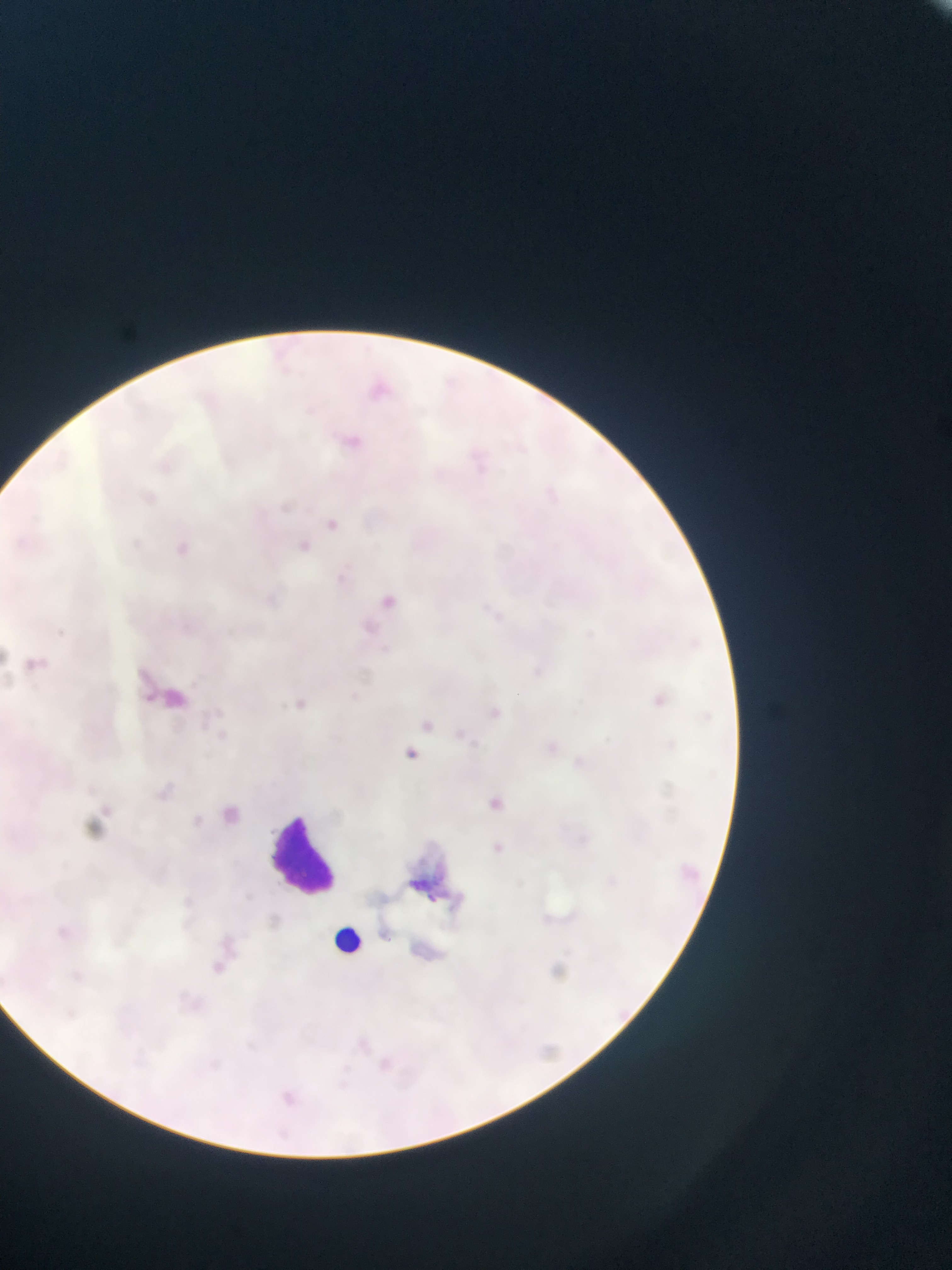

Approximate bounding boxes as {left, top, right, bottom} in pixels. Leukocyte locations: {262, 802, 351, 891}, {327, 917, 375, 964}. Artifact (stain precipitate or debris) locations: {396, 837, 475, 921}. Single field of view. Image is 952×1270 pixels. Collected in Ghana. Thin blood film. Mobile-phone photograph taken through the microscope.